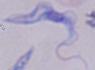

Summary:
  - Identification: trypanosome
  - Magnification: 1000x
  - Modality: micrograph